Classify this cell by malaria status.
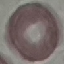
Uninfected.

preparation = thin smear
stain = Giemsa
capture = smartphone through the microscope eyepiece
image type = automatically extracted cell patch, resized to 64 × 64 pixels